State which cell type is depicted.
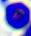

A leukocyte.

modality = photomicrograph
magnification = 400x